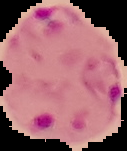

malaria status = parasitized
image size = 127×151 pixels
image type = cell region segmented out of the field of view; surrounding area masked to black
preparation = thin blood film